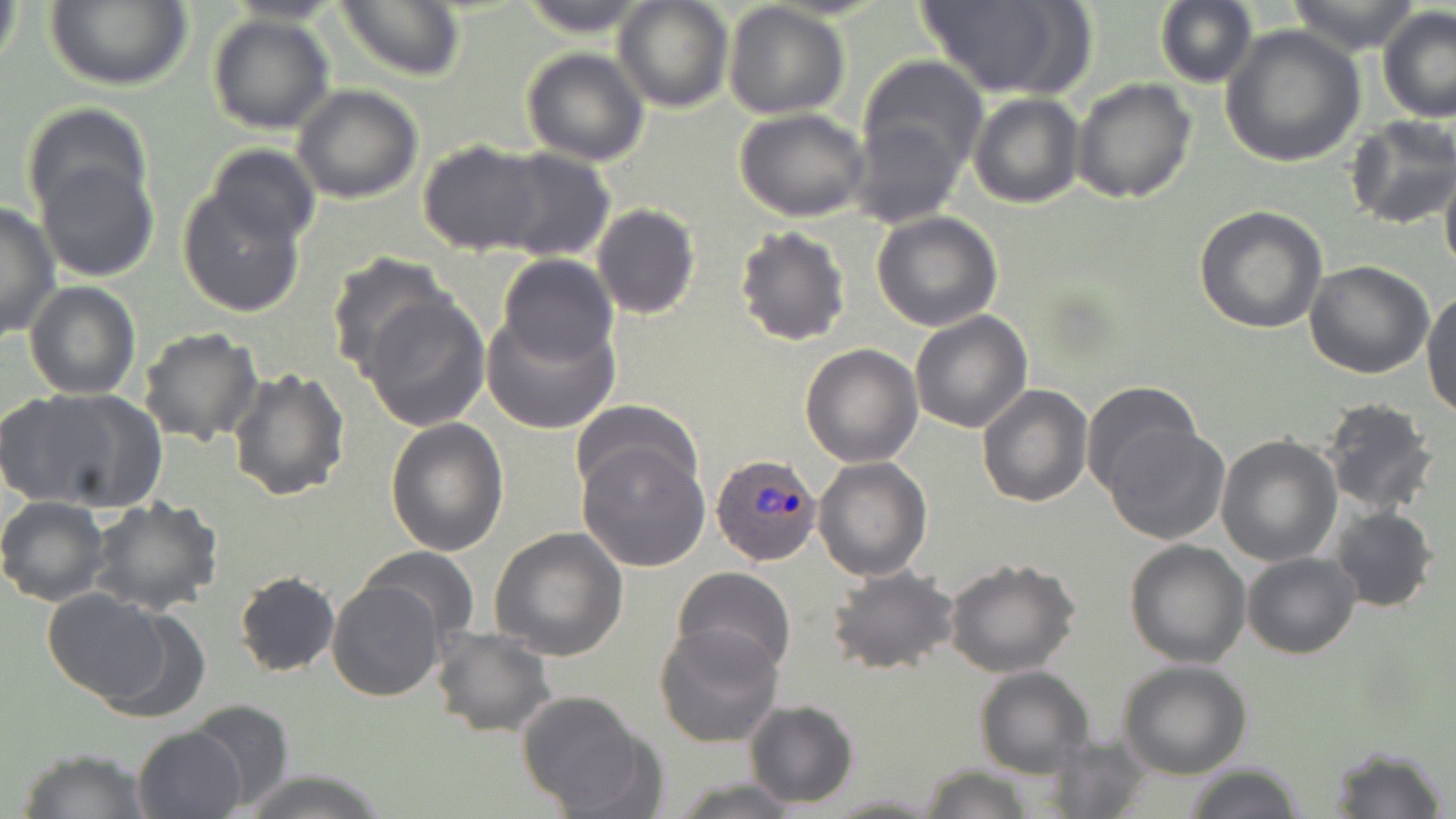
Approximate bounding boxes as (x1, y1, x2, y2) in pixels. Uninfected red blood cell locations: (0, 0, 22, 87), (223, 0, 347, 24), (334, 0, 466, 82), (516, 0, 654, 36), (613, 0, 734, 112), (915, 0, 1088, 98), (1285, 0, 1423, 54), (44, 1, 192, 90), (1154, 1, 1257, 88), (723, 2, 851, 121), (1376, 7, 1455, 124), (207, 14, 335, 134), (1220, 25, 1365, 167), (521, 47, 649, 165), (857, 54, 988, 191), (1071, 79, 1197, 204), (291, 85, 423, 204), (968, 92, 1085, 209), (21, 103, 152, 220), (734, 109, 871, 222), (1345, 115, 1456, 230), (417, 140, 550, 256), (204, 144, 321, 248), (490, 146, 615, 263), (36, 157, 160, 283), (1440, 159, 1456, 282), (176, 184, 307, 317), (0, 201, 59, 341), (590, 203, 699, 319), (1195, 206, 1328, 334), (871, 212, 1004, 332), (734, 225, 852, 348), (323, 251, 452, 379), (496, 253, 618, 368), (1304, 260, 1435, 379), (24, 281, 142, 401), (1423, 288, 1456, 418), (362, 294, 490, 430), (483, 309, 618, 435), (909, 310, 1033, 434), (138, 327, 264, 445), (799, 343, 923, 467), (227, 367, 350, 504), (1081, 381, 1201, 497), (977, 384, 1092, 507), (7, 388, 163, 513), (1318, 397, 1439, 516), (571, 399, 700, 500), (385, 418, 509, 558), (1104, 425, 1228, 545), (1215, 436, 1341, 567), (578, 441, 711, 571), (812, 457, 932, 580), (0, 496, 110, 606), (89, 496, 223, 617), (1329, 507, 1438, 614), (489, 527, 629, 662), (1124, 538, 1252, 668), (360, 547, 479, 644), (1242, 552, 1360, 658), (943, 561, 1081, 678), (673, 566, 797, 679), (826, 566, 960, 675), (234, 572, 340, 677), (328, 579, 444, 701), (42, 588, 173, 705), (654, 624, 785, 749), (432, 628, 557, 738), (1118, 659, 1252, 779), (974, 666, 1094, 777), (515, 690, 655, 815), (186, 699, 293, 810), (744, 701, 859, 810), (132, 725, 249, 819), (1325, 745, 1448, 819), (16, 747, 150, 819), (1182, 763, 1307, 819), (920, 765, 1035, 819), (236, 770, 392, 819), (666, 779, 803, 818), (823, 792, 945, 817). Plasmodium ovale-infected red blood cell locations: (710, 454, 823, 568). Slide-level diagnosis: Plasmodium ovale. May-Grünwald-Giemsa-stained preparation. Single field of view. Thin blood smear. Light microscopy. Image is 1456×819 pixels. 1000x magnification.